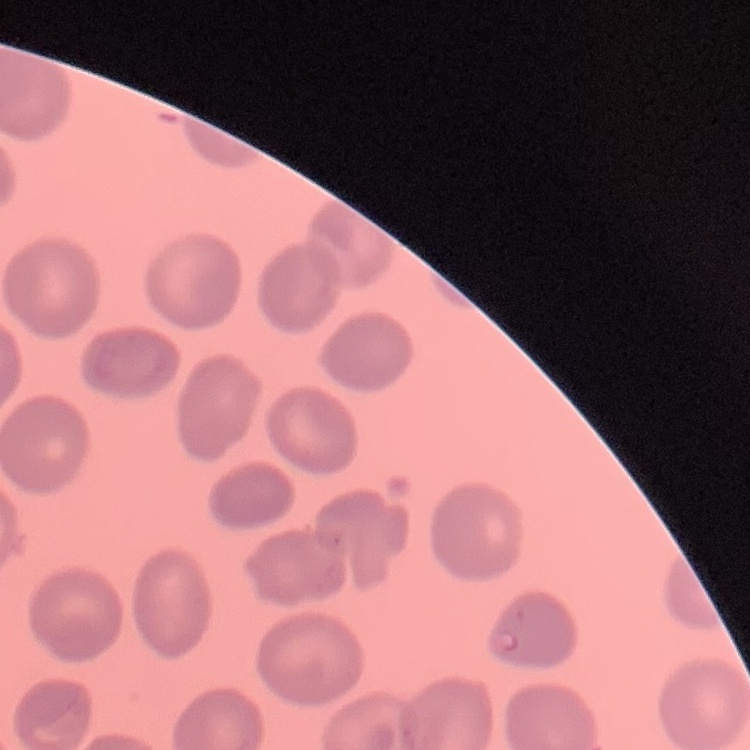
The erythrocytes show no rouleaux formation. Square crop of a larger photomicrograph. Field's or Giemsa stain. Thin blood smear.